State the blood parasite species.
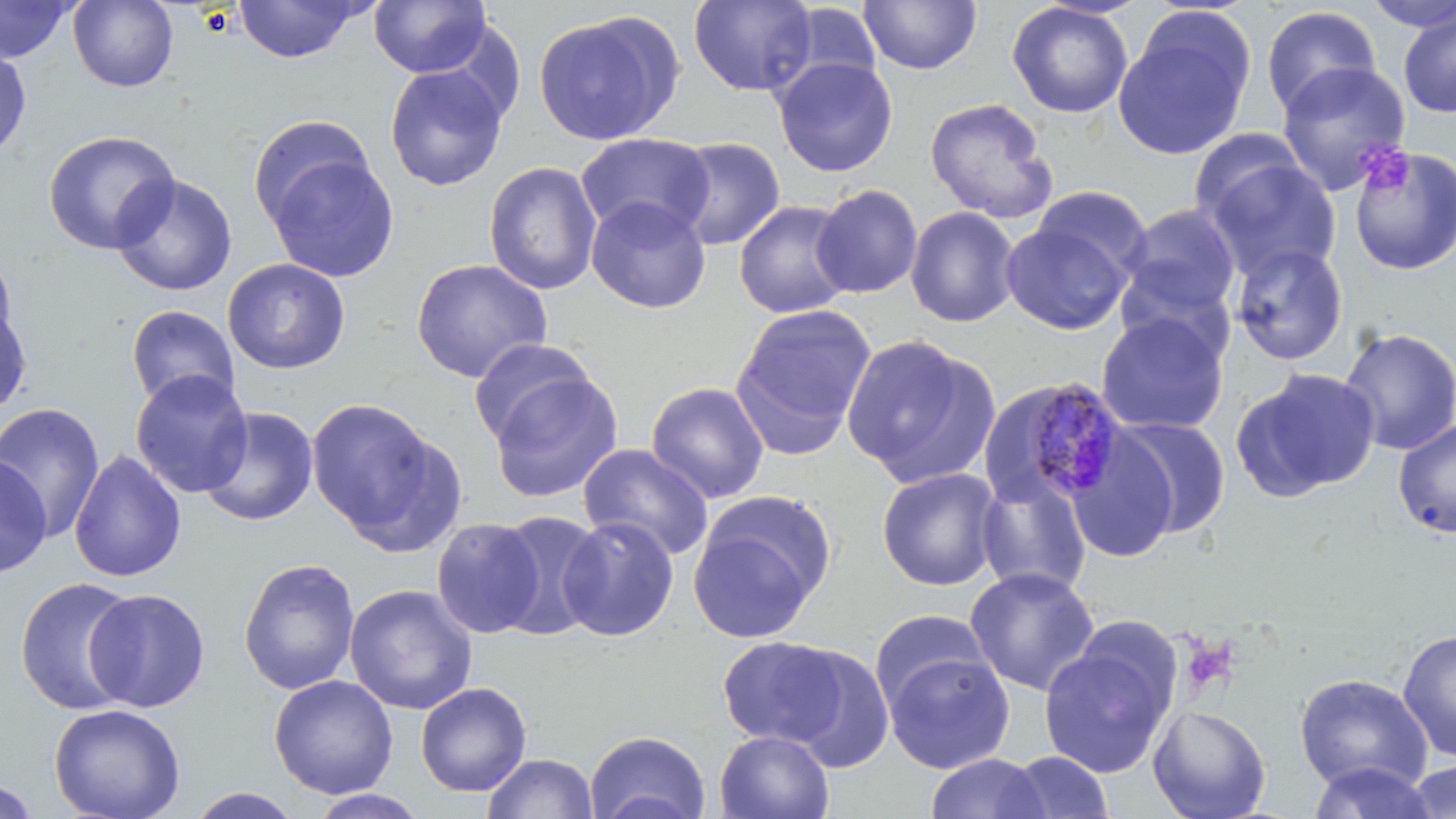

Plasmodium malariae.

Approximate bounding boxes as (x1,y1)-(x2,y2) corner pairs in pixels. Platelet locations: (1355,144)-(1413,195). Uninfected red blood cell locations: (0,0)-(77,64), (368,0)-(490,76), (688,0)-(818,97), (858,0)-(983,75), (67,1)-(179,92), (233,1)-(369,64), (1361,1)-(1456,32), (779,2)-(884,94), (1006,2)-(1133,118), (1260,5)-(1381,118), (1398,8)-(1456,119), (532,10)-(681,146), (1114,15)-(1254,161), (0,46)-(32,161), (773,56)-(898,177), (1276,61)-(1412,196), (384,64)-(509,192), (925,97)-(1058,224), (246,113)-(378,229), (42,129)-(180,255), (1189,129)-(1310,228), (576,132)-(715,242), (670,137)-(786,252), (1349,146)-(1456,276), (264,153)-(400,283), (1203,155)-(1341,281), (484,161)-(602,295), (110,173)-(238,297), (811,184)-(923,299), (1031,185)-(1151,282), (586,196)-(712,314), (733,200)-(855,319), (1121,203)-(1242,318), (904,206)-(1021,328), (1001,221)-(1132,335), (1230,243)-(1348,366), (0,247)-(19,356), (221,258)-(351,375), (410,258)-(552,383), (1115,262)-(1237,368), (731,302)-(876,451), (0,303)-(33,416), (125,305)-(240,410), (1096,312)-(1229,435), (1337,326)-(1455,456), (842,335)-(998,486), (469,337)-(598,447), (1235,368)-(1380,501), (130,369)-(254,498), (487,370)-(624,503), (646,382)-(769,503), (307,399)-(442,539), (0,402)-(105,542), (198,406)-(319,528), (1114,417)-(1231,538), (1393,418)-(1456,539), (1065,429)-(1180,565), (577,443)-(714,561), (69,450)-(187,583), (0,455)-(52,578), (876,467)-(1003,591), (975,473)-(1092,598), (689,495)-(834,644), (491,510)-(607,641), (557,515)-(679,642), (431,517)-(545,638), (386,534)-(523,680), (238,557)-(360,695), (964,566)-(1100,696), (15,577)-(140,715), (344,584)-(478,715), (83,588)-(210,712), (869,609)-(994,714), (1397,629)-(1456,763), (716,635)-(850,748), (1038,641)-(1175,779), (782,648)-(896,773), (882,649)-(1015,774), (1294,672)-(1433,795), (268,675)-(398,799), (416,682)-(531,797), (48,703)-(186,819), (1148,703)-(1271,819), (585,730)-(710,819), (714,730)-(835,818), (1004,750)-(1114,818), (481,752)-(598,818), (925,752)-(1049,818), (1403,759)-(1456,819), (1305,761)-(1441,819), (0,777)-(41,818), (186,787)-(304,818), (308,789)-(430,818). Plasmodium malariae-infected red blood cell locations: (1023,376)-(1130,508). Image is 1456×819 pixels. Optical microscopy. Thin blood smear. Captured at 1000x magnification. Single field of view. May-Grünwald-Giemsa-stained preparation.